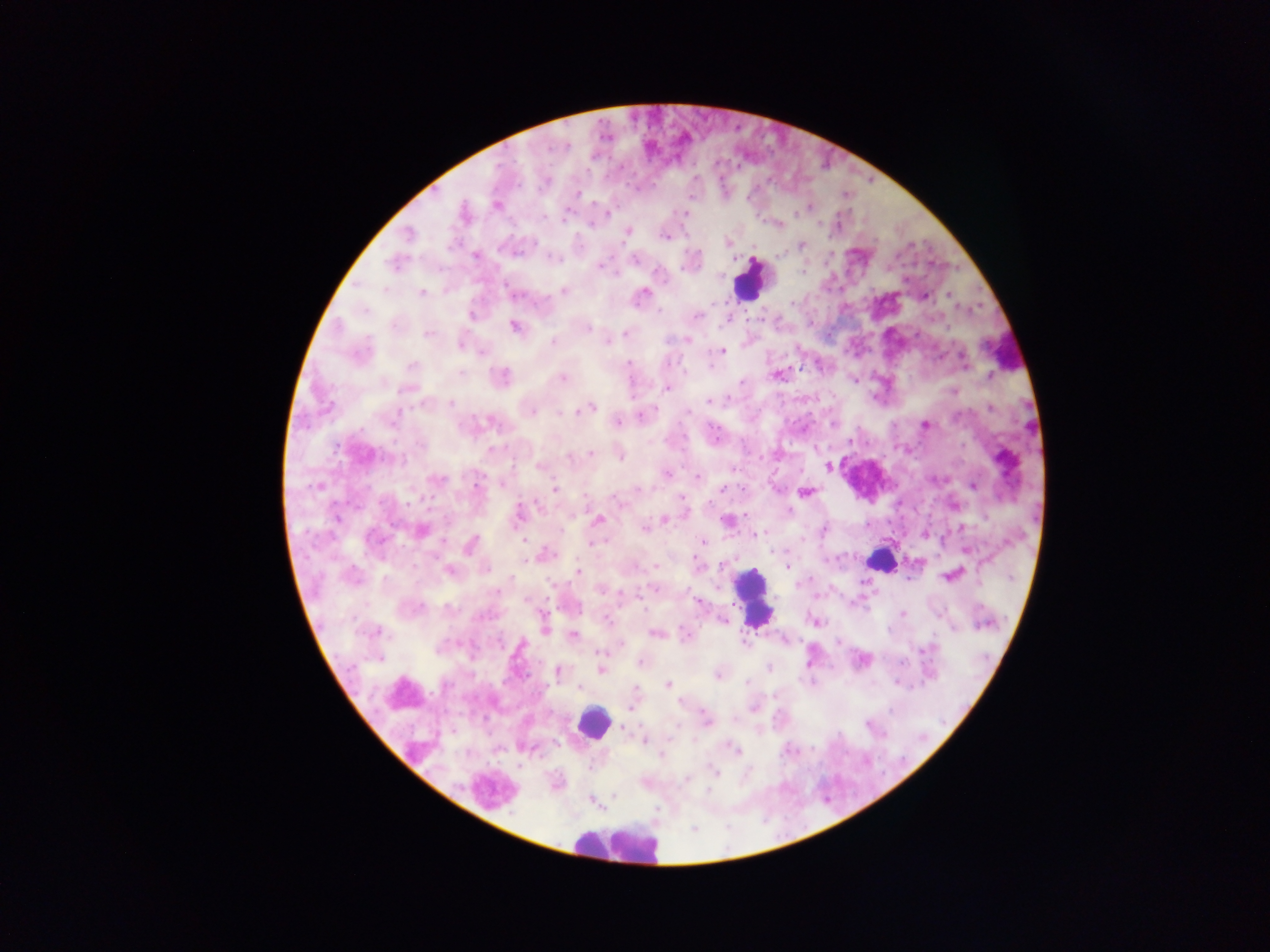

malaria parasite locations = approximate centers as {x, y} in pixels: {736, 129}, {515, 161}, {693, 163}, {718, 163}, {589, 168}, {741, 170}, {696, 178}, {770, 180}, {869, 181}, {519, 182}, {724, 184}, {432, 188}, {542, 191}, {576, 194}, {847, 195}, {691, 196}, {750, 196}, {496, 205}, {813, 207}, {796, 211}, {551, 212}, {565, 212}, {608, 213}, {685, 213}, {463, 214}, {756, 215}, {589, 223}, {778, 224}, {822, 225}, {627, 230}, {406, 234}, {666, 235}, {832, 237}, {877, 239}, {727, 242}, {800, 245}, {523, 249}, {699, 254}, {476, 256}, {553, 257}, {835, 257}, {612, 258}, {636, 260}, {394, 263}, {828, 264}, {932, 264}, {598, 265}, {681, 268}, {659, 270}, {804, 270}, {906, 276}, {507, 286}, {872, 287}, {564, 291}, {421, 292}, {524, 293}, {641, 294}, {924, 296}, {949, 296}, {796, 301}, {714, 302}, {660, 308}, {472, 313}, {697, 314}, {727, 319}, {748, 319}, {762, 319}, {813, 325}, {515, 327}, {587, 328}, {428, 332}, {626, 333}, {830, 335}, {687, 339}, {553, 341}, {607, 341}, {461, 344}, {872, 346}, {722, 351}, {627, 360}, {715, 364}, {803, 370}, {777, 374}, {988, 375}, {500, 377}, {561, 377}, {853, 380}, {739, 384}, {666, 388}, {954, 391}, {731, 397}, {709, 401}, {454, 402}, {988, 407}, {560, 408}, {587, 408}, {530, 410}, {644, 415}, {691, 415}, {617, 422}, {834, 425}, {924, 425}, {393, 428}, {363, 430}, {717, 436}, {687, 439}, {851, 439}, {508, 445}, {794, 450}, {335, 452}, {590, 454}, {619, 455}, {762, 457}, {540, 467}, {827, 467}, {666, 472}, {697, 477}, {437, 479}, {475, 484}, {502, 484}, {972, 485}, {318, 486}, {555, 488}, {638, 488}, {722, 489}, {805, 492}, {585, 495}, {433, 496}, {616, 497}, {681, 497}, {423, 500}, {335, 501}, {933, 503}, {408, 504}, {381, 505}, {517, 515}, {337, 518}, {664, 519}, {598, 521}, {726, 521}, {869, 523}, {392, 524}, {889, 524}, {562, 528}, {645, 528}, {420, 530}, {822, 530}, {907, 534}, {924, 534}, {752, 535}, {525, 538}, {445, 541}, {701, 541}, {591, 544}, {471, 545}, {317, 546}, {965, 550}, {543, 555}, {839, 558}, {355, 560}, {913, 561}, {697, 563}, {655, 566}, {787, 566}, {448, 570}, {578, 571}, {813, 575}, {950, 575}, {514, 580}, {600, 588}, {639, 590}, {832, 590}, {697, 600}, {548, 601}, {869, 606}, {646, 608}, {901, 614}, {355, 616}, {543, 619}, {723, 621}, {814, 621}, {543, 629}, {375, 631}, {655, 632}, {572, 635}, {784, 640}, {843, 640}, {621, 644}, {600, 654}, {383, 657}, {813, 659}, {862, 659}, {639, 662}, {769, 667}, {601, 668}, {558, 671}, {529, 672}, {718, 674}, {504, 678}, {893, 680}, {667, 685}, {579, 686}, {432, 690}, {632, 706}, {753, 707}, {890, 707}, {484, 717}, {706, 719}, {778, 722}, {868, 725}, {452, 731}, {645, 740}, {813, 743}, {731, 747}, {783, 755}, {904, 756}, {714, 772}, {886, 776}, {687, 779}, {615, 796}, {591, 799}
preparation = thick blood film
field of view = single
country = Ghana
capture = mobile-phone photograph through a microscope
leukocyte locations = approximate centers as {x, y} in pixels: {749, 278}, {1004, 347}, {871, 476}, {881, 560}, {754, 597}, {592, 723}, {492, 790}, {617, 845}
image size = 1270×952 pixels